Report the malaria status.
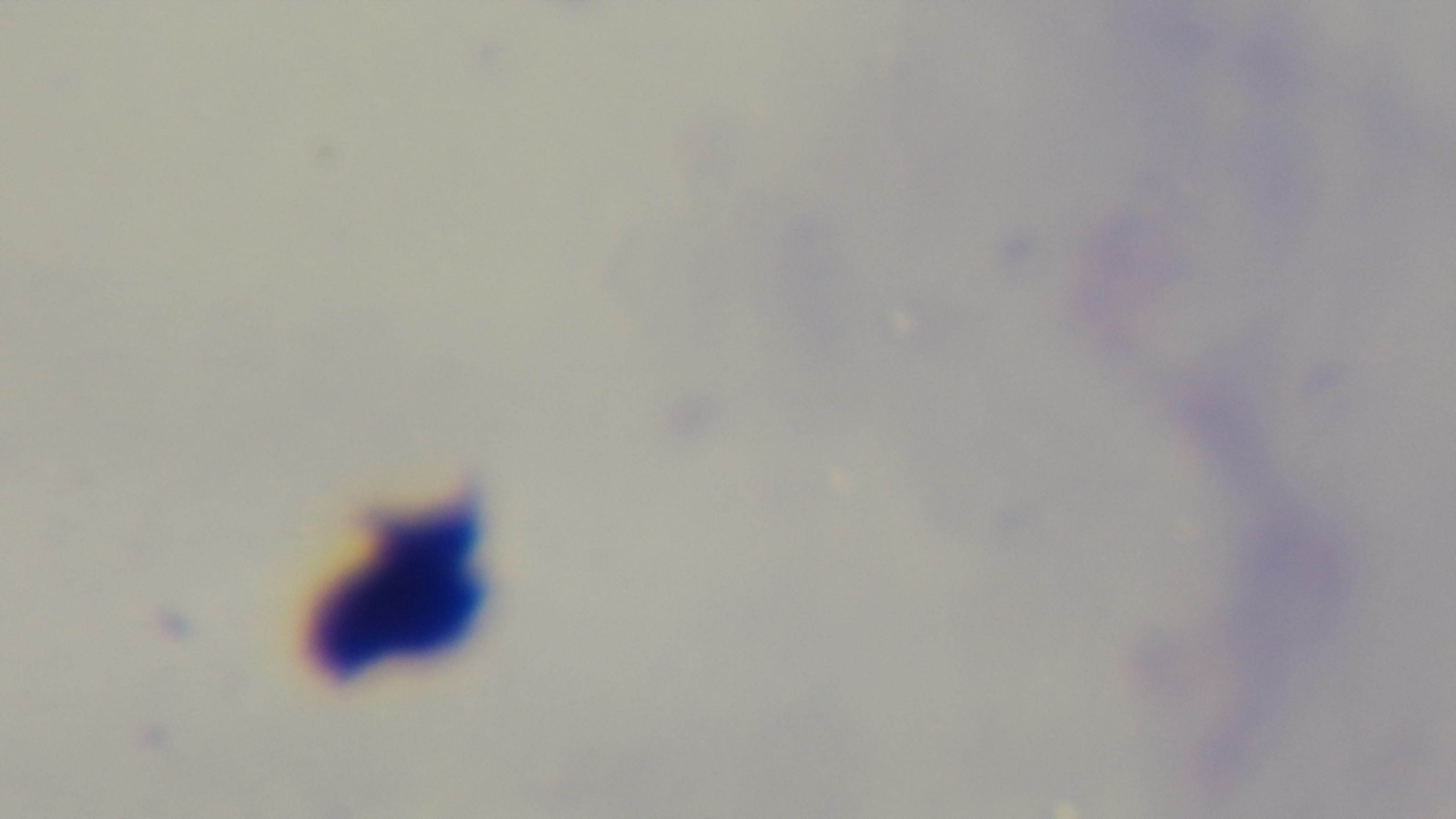
Negative.

100x oil-immersion objective. Light microscopy. Giemsa-stained. Mounted 4K digital camera. Preparation: thick. One field from the slide.